Describe the morphology of the erythrocytes.
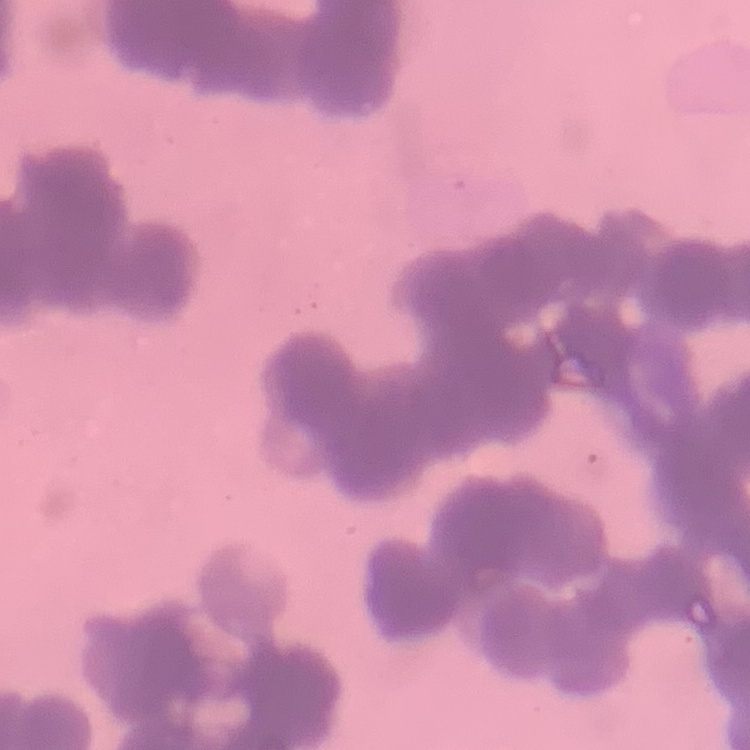

Rouleaux formation.

Summary:
  - Preparation: thin blood smear
  - Stain: Field's or Giemsa
  - Image type: one tile cut from a larger photomicrograph